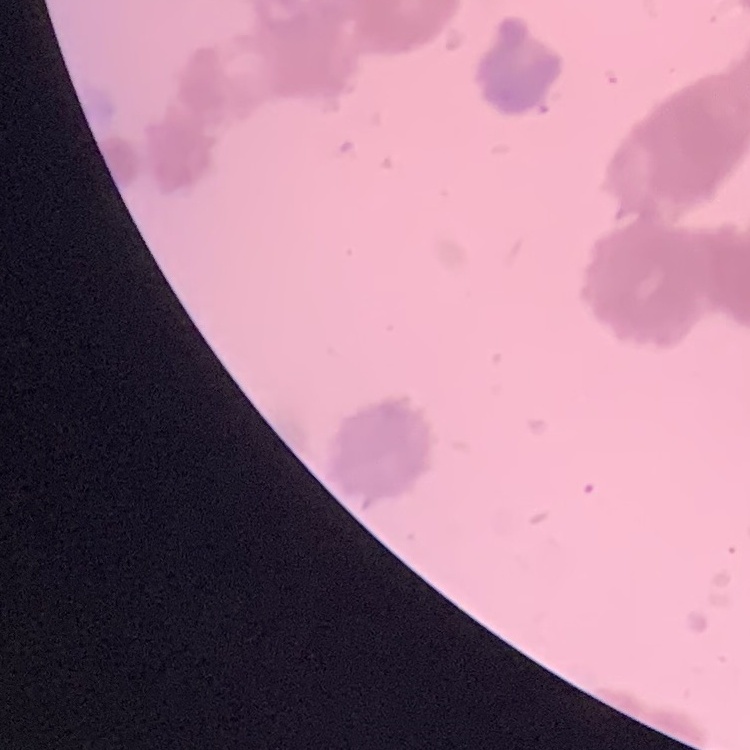

{
  "red_blood_cell_morphology": "rouleaux formation",
  "preparation": "thin peripheral smear",
  "image_type": "one tile cut from a larger photomicrograph",
  "stain": "Field's or Giemsa"
}